Locate every Plasmodium falciparum-infected red blood cell.
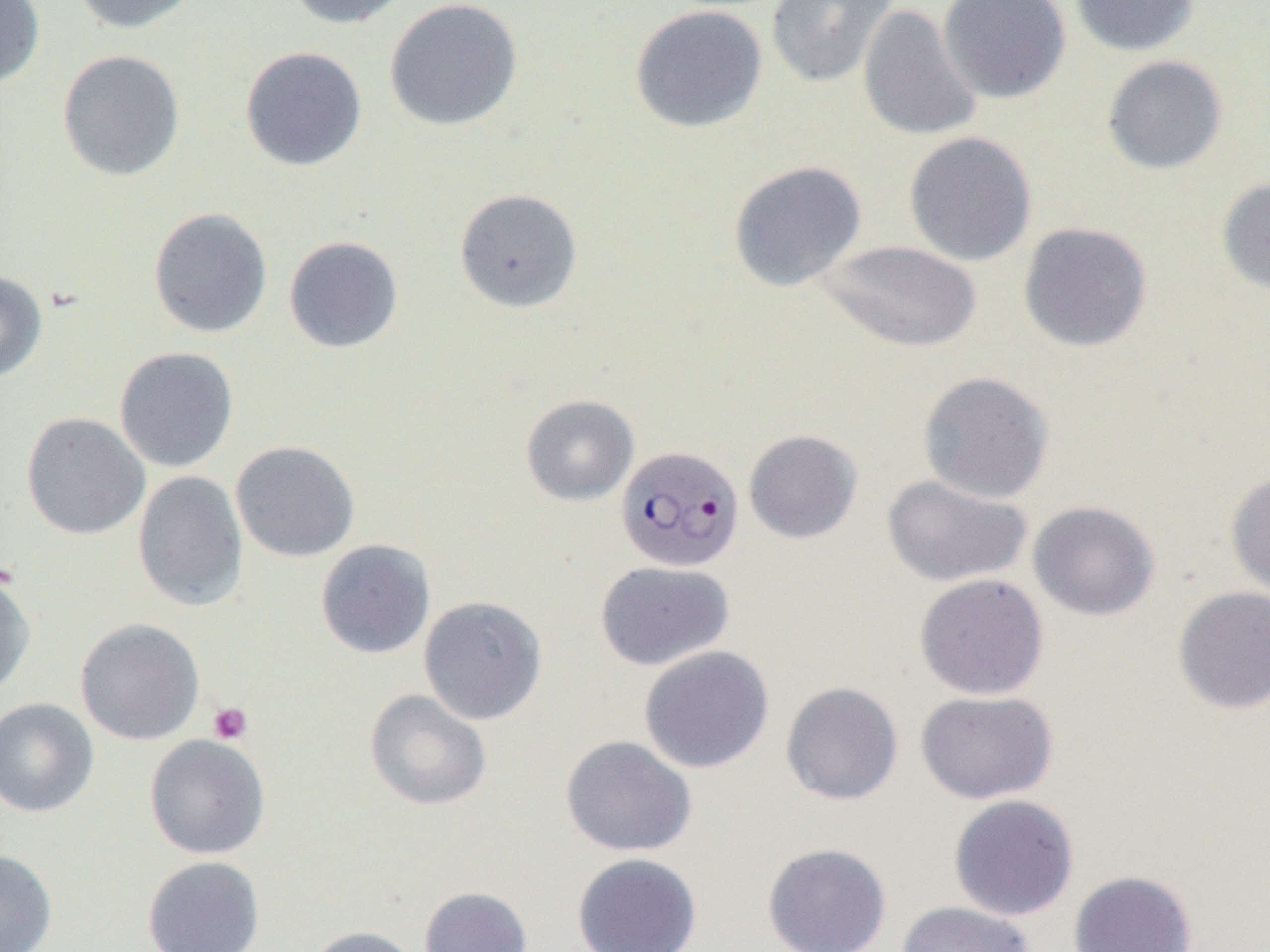

Approximate bounding boxes as named x1/y1/x2/y2 corners in pixels.
Plasmodium falciparum-infected red blood cells: (x1=615, y1=444, x2=743, y2=572).

Summary:
  - Platelet locations: (x1=207, y1=701, x2=252, y2=744)
  - Uninfected red blood cell locations: (x1=0, y1=0, x2=45, y2=87), (x1=70, y1=0, x2=205, y2=34), (x1=283, y1=0, x2=415, y2=28), (x1=384, y1=0, x2=523, y2=132), (x1=765, y1=0, x2=897, y2=87), (x1=937, y1=0, x2=1071, y2=104), (x1=1070, y1=0, x2=1201, y2=57), (x1=857, y1=3, x2=982, y2=142), (x1=630, y1=4, x2=768, y2=133), (x1=239, y1=46, x2=367, y2=172), (x1=56, y1=49, x2=186, y2=182), (x1=1101, y1=55, x2=1228, y2=174), (x1=903, y1=131, x2=1038, y2=266), (x1=728, y1=160, x2=867, y2=292), (x1=1216, y1=176, x2=1270, y2=296), (x1=454, y1=188, x2=583, y2=313), (x1=148, y1=207, x2=273, y2=338), (x1=1017, y1=221, x2=1153, y2=353), (x1=283, y1=236, x2=403, y2=353), (x1=816, y1=239, x2=983, y2=353), (x1=0, y1=270, x2=48, y2=383), (x1=114, y1=346, x2=239, y2=473), (x1=917, y1=371, x2=1054, y2=504), (x1=521, y1=394, x2=639, y2=506), (x1=21, y1=412, x2=150, y2=539), (x1=743, y1=429, x2=863, y2=544), (x1=230, y1=440, x2=360, y2=562), (x1=1225, y1=469, x2=1270, y2=600), (x1=132, y1=470, x2=248, y2=611), (x1=881, y1=474, x2=1033, y2=587), (x1=1028, y1=500, x2=1160, y2=621), (x1=315, y1=539, x2=436, y2=659), (x1=595, y1=560, x2=734, y2=670), (x1=0, y1=571, x2=36, y2=698), (x1=914, y1=573, x2=1049, y2=700), (x1=1172, y1=586, x2=1270, y2=714), (x1=418, y1=595, x2=547, y2=725), (x1=75, y1=617, x2=205, y2=746), (x1=639, y1=645, x2=774, y2=773), (x1=781, y1=681, x2=903, y2=805), (x1=364, y1=689, x2=492, y2=811), (x1=916, y1=690, x2=1058, y2=804), (x1=0, y1=697, x2=99, y2=817), (x1=144, y1=734, x2=271, y2=859), (x1=560, y1=735, x2=697, y2=857), (x1=948, y1=794, x2=1080, y2=921), (x1=762, y1=842, x2=892, y2=952), (x1=0, y1=849, x2=57, y2=952), (x1=572, y1=853, x2=703, y2=952), (x1=142, y1=855, x2=266, y2=951), (x1=1068, y1=870, x2=1197, y2=952), (x1=418, y1=886, x2=533, y2=952), (x1=896, y1=901, x2=1036, y2=952), (x1=303, y1=925, x2=423, y2=952)
  - Slide-level diagnosis: Plasmodium falciparum
  - Magnification: 1000x
  - Image size: 1270×952 pixels
  - Field of view: single
  - Modality: light microscopy
  - Preparation: thin blood film